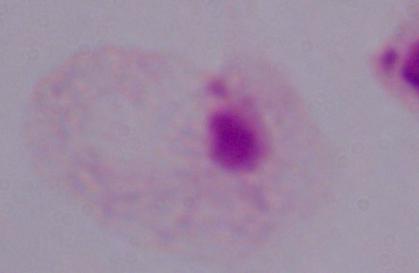

A trichomonad is shown. Micrograph. Captured at 1000x magnification.